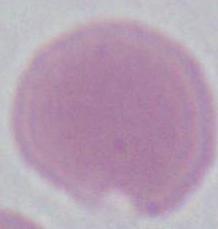

Micrograph. An erythrocyte is seen. Captured at 1000x magnification.